Identify the cell.
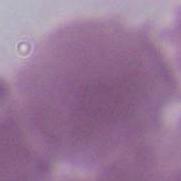
This is an erythrocyte.

modality = photomicrograph
magnification = 1000x